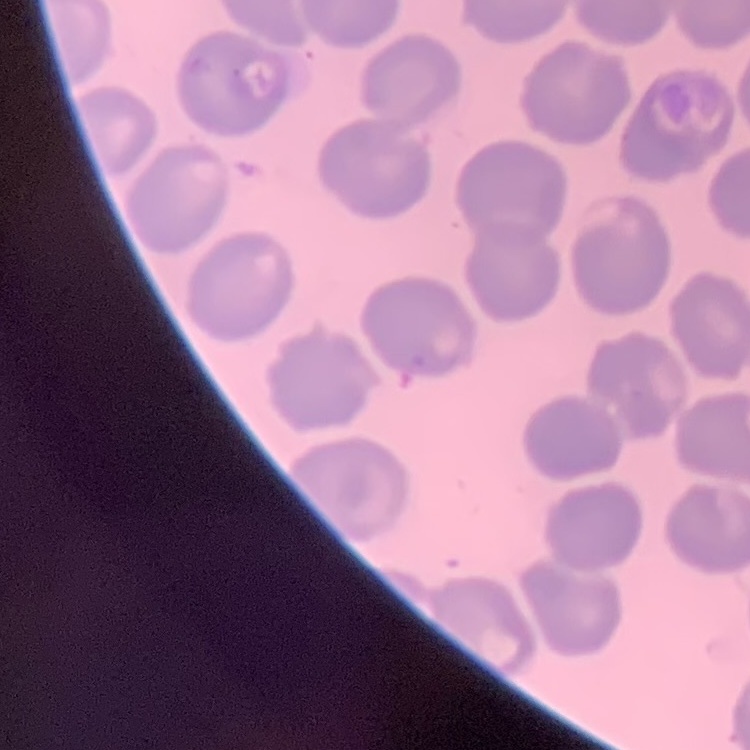
red blood cell morphology = no rouleaux formation
image type = one tile cut from a larger photomicrograph
preparation = thin blood film
stain = Field's or Giemsa